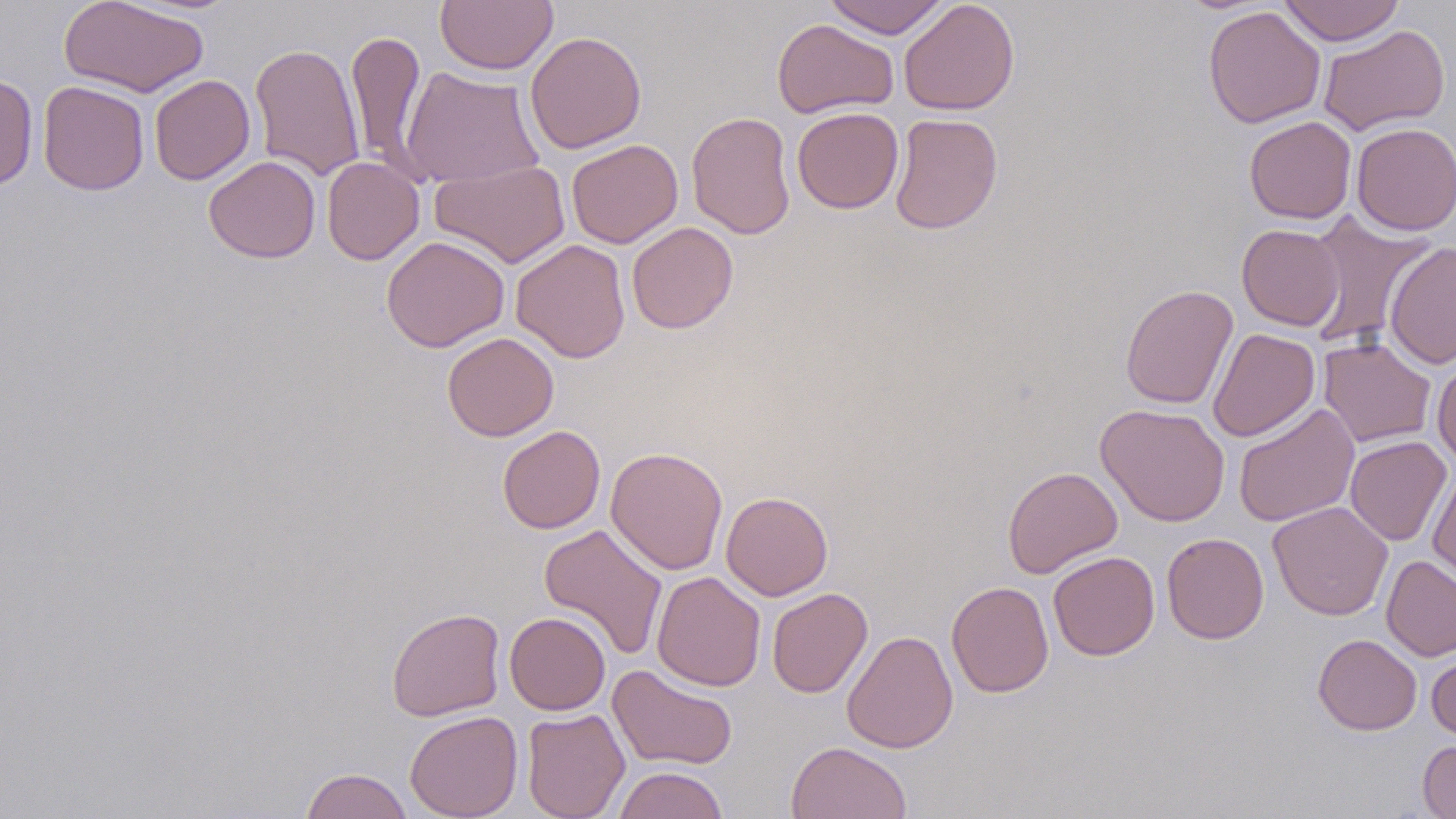
slide_level_diagnosis: negative for blood parasites
field_of_view: one of a larger specimen
modality: optical microscopy
stain: May-Grünwald-Giemsa
preparation: thin blood film
uninfected_red_blood_cell_locations: 'approximate bounding boxes as (x1, y1, x2, y2) in pixels: (57, 0, 210, 98), (434, 0, 558, 75), (822, 0, 950, 38), (899, 0, 1020, 116), (1278, 0, 1405, 46), (1203, 6, 1326, 128), (772, 18, 898, 119), (1317, 25, 1450, 136), (346, 30, 427, 174), (524, 31, 647, 153), (249, 43, 366, 181), (399, 66, 544, 188), (0, 74, 39, 192), (150, 74, 255, 185), (38, 81, 150, 195), (791, 106, 904, 214), (686, 111, 796, 240), (889, 112, 1003, 235), (1244, 116, 1357, 224), (1351, 122, 1456, 235), (566, 139, 683, 249), (204, 156, 320, 263), (322, 157, 425, 265), (430, 160, 571, 268), (1302, 211, 1437, 349), (626, 221, 739, 334), (1237, 224, 1344, 331), (381, 236, 510, 352), (510, 239, 631, 363), (1386, 241, 1456, 369), (1120, 283, 1238, 410), (1207, 328, 1320, 442), (442, 332, 559, 442), (1318, 337, 1436, 447), (1432, 357, 1456, 467), (1095, 403, 1230, 526), (1233, 403, 1360, 527), (497, 425, 605, 533), (1345, 436, 1451, 546), (605, 446, 729, 575), (1002, 466, 1123, 579), (1427, 468, 1456, 588), (720, 491, 833, 600), (1267, 501, 1393, 621), (538, 523, 668, 660), (1161, 533, 1269, 644), (1048, 551, 1160, 660), (1381, 555, 1456, 662), (651, 571, 766, 691), (947, 581, 1054, 697), (767, 588, 872, 698), (386, 607, 506, 722), (505, 611, 610, 715), (842, 630, 959, 754), (1313, 634, 1421, 735), (1426, 650, 1456, 742), (608, 664, 737, 771), (521, 708, 630, 819), (405, 710, 523, 819), (1417, 739, 1456, 818), (785, 741, 912, 819), (614, 766, 728, 819), (299, 767, 414, 819)'
magnification: 1000x
image_size: 1456×819 pixels